Name the parasite shown.
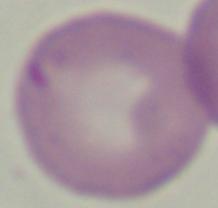

This is Babesia.

1000x magnification. Photomicrograph.